Comment on the morphology of the red blood cells.
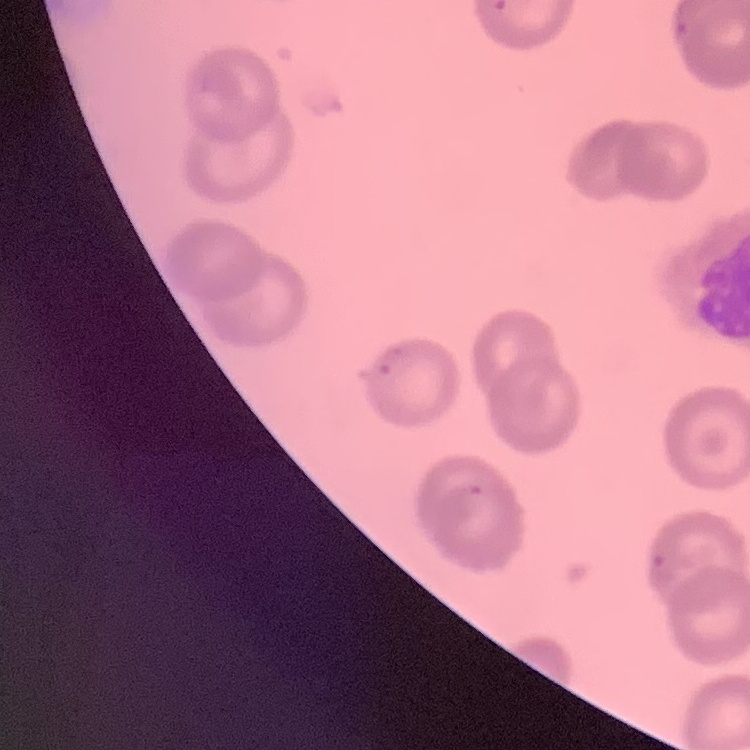

No rouleaux formation.

Field's or Giemsa stain. Thin blood film. Square crop of a larger photomicrograph.